Describe the morphology of the red blood cells.
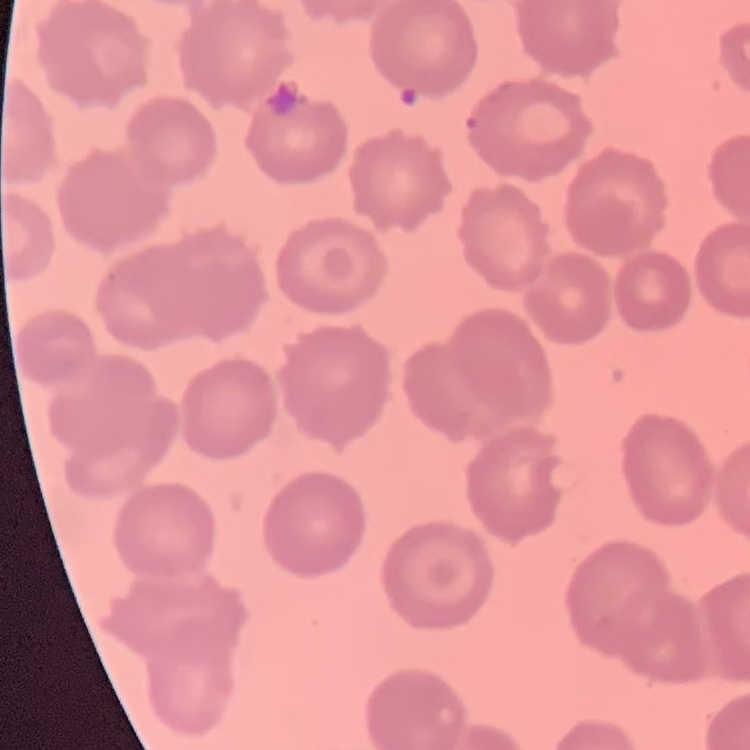

No rouleaux formation.

Square crop of a larger photomicrograph. Thin blood film. Field's or Giemsa stain.